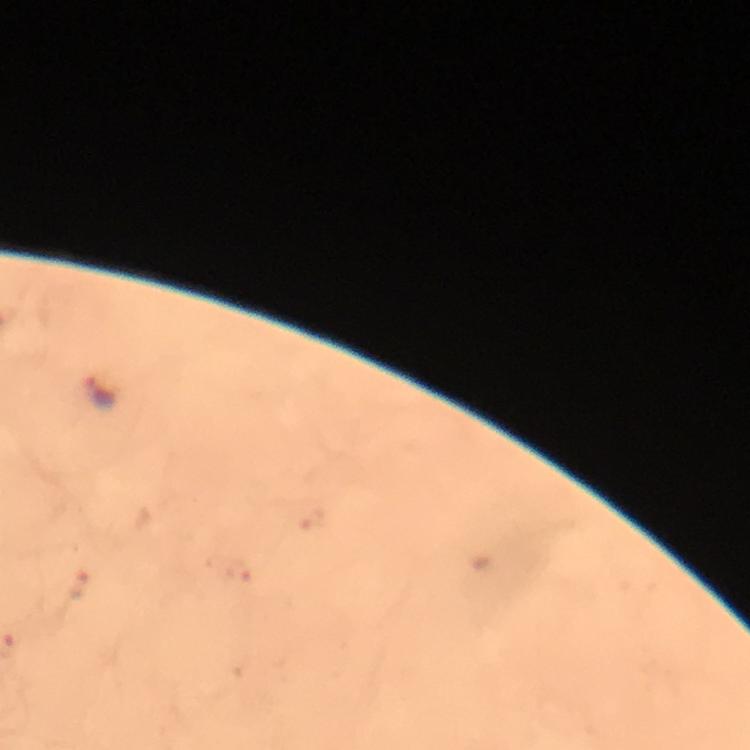
stain: Giemsa
malaria_parasite_locations: 'approximate centers as {x, y} in pixels: {101, 393}, {80, 587}'
preparation: thick blood film
capture: smartphone mounted on the microscope
magnification: 100x
cropped_from: one field of view
context: from a malaria diagnostic workup
image_size: 750×750 pixels
immersion_oil: used